Outline each Plasmodium malariae-infected red blood cell.
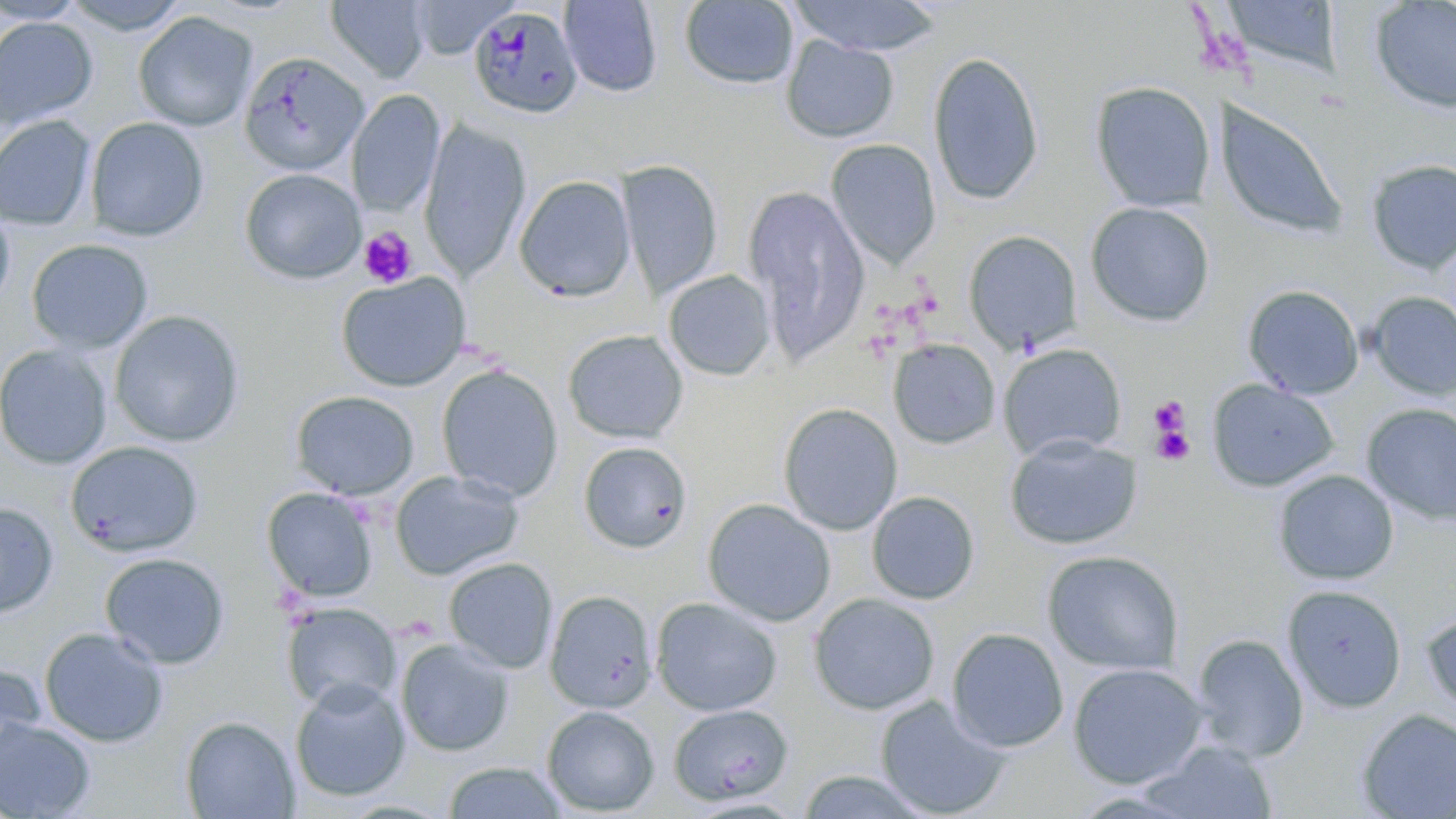

Approximate bounding boxes as (x1, y1, x2, y2) in pixels.
Plasmodium malariae-infected red blood cells: (468, 5, 584, 120).

Platelet locations: (358, 227, 417, 288), (1149, 397, 1190, 445), (1149, 415, 1194, 467). Uninfected red blood cell locations: (59, 0, 193, 35), (326, 0, 430, 83), (558, 0, 663, 97), (787, 0, 941, 56), (1370, 0, 1456, 114), (0, 1, 90, 24), (405, 1, 519, 59), (679, 1, 799, 90), (332, 2, 435, 167), (1221, 2, 1343, 81), (133, 11, 258, 132), (0, 16, 98, 131), (780, 34, 899, 143), (238, 51, 369, 176), (927, 51, 1045, 206), (1090, 81, 1216, 213), (347, 89, 446, 218), (1213, 99, 1347, 240), (0, 115, 97, 230), (85, 116, 210, 242), (419, 119, 531, 281), (825, 138, 941, 269), (1366, 159, 1456, 275), (617, 160, 723, 299), (239, 168, 366, 285), (514, 175, 636, 301), (744, 186, 871, 363), (0, 201, 15, 314), (1085, 202, 1215, 327), (963, 230, 1082, 353), (26, 239, 154, 354), (663, 270, 775, 381), (336, 272, 470, 392), (1242, 285, 1364, 399), (1366, 291, 1456, 400), (108, 310, 246, 447), (562, 329, 688, 444), (888, 340, 1000, 449), (998, 343, 1127, 461), (0, 345, 113, 469), (436, 365, 563, 502), (1206, 379, 1339, 492), (290, 390, 418, 500), (777, 403, 903, 536), (1361, 404, 1456, 526), (1004, 434, 1142, 550), (65, 441, 204, 558), (577, 441, 694, 554), (389, 469, 525, 581), (1272, 469, 1399, 585), (261, 486, 379, 602), (866, 491, 981, 605), (701, 498, 836, 627), (0, 502, 59, 618), (1042, 550, 1184, 676), (99, 552, 230, 670), (443, 557, 558, 674), (1282, 584, 1407, 714), (545, 590, 657, 713), (808, 593, 940, 715), (650, 596, 782, 716), (280, 602, 401, 714), (1421, 609, 1456, 718), (39, 626, 169, 747), (946, 627, 1069, 752), (1190, 634, 1309, 761), (396, 637, 515, 757), (0, 660, 46, 767), (1068, 662, 1209, 789), (289, 679, 410, 802), (875, 695, 1010, 818), (668, 704, 795, 805), (541, 705, 659, 816), (1355, 708, 1456, 819), (180, 716, 299, 818), (0, 717, 96, 818), (1140, 740, 1279, 818), (441, 761, 569, 819), (796, 769, 933, 819). Slide-level diagnosis: Plasmodium malariae. Optical microscopy. Image is 1456×819 pixels. May-Grünwald-Giemsa-stained preparation. Thin blood smear. Captured at 1000x magnification. Single field of view.